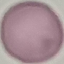

result: no malaria parasites seen
capture: smartphone camera at the microscope eyepiece
stain: Giemsa
preparation: thin blood film
image_type: cell patch, automatically extracted from a larger field of view and resized to 64 × 64 pixels